Mark where platelets are.
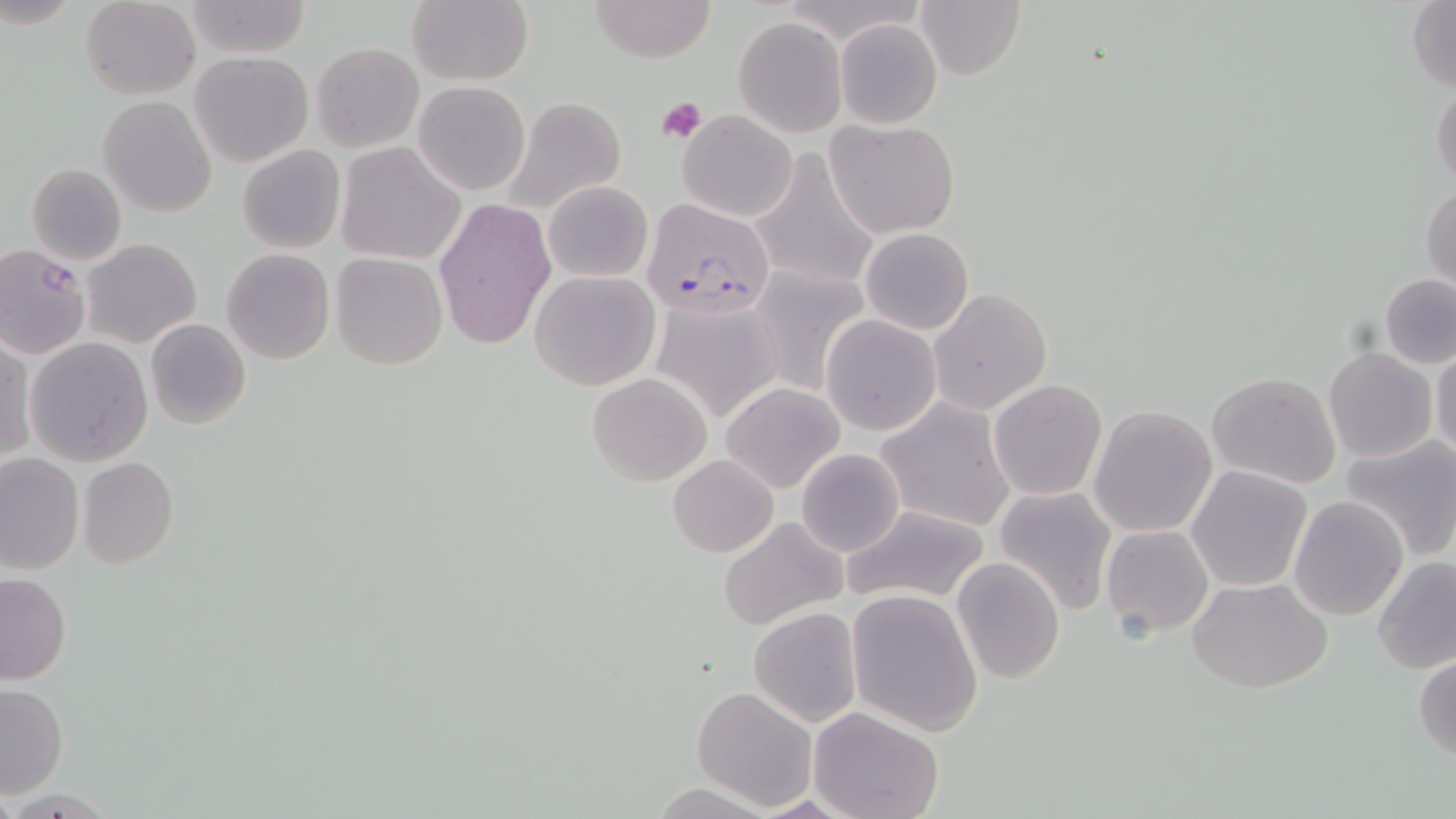
Approximate bounding boxes as [x1, y1, x2, y2] in pixels.
Platelets: [655, 95, 707, 144].

Uninfected red blood cell locations: [79, 0, 201, 99], [406, 0, 533, 86], [586, 0, 717, 62], [183, 1, 310, 61], [915, 1, 1025, 81], [1405, 1, 1455, 93], [732, 17, 847, 137], [833, 18, 942, 129], [311, 42, 423, 152], [190, 52, 314, 166], [414, 81, 530, 196], [1430, 81, 1456, 191], [98, 96, 216, 217], [500, 96, 629, 214], [676, 109, 798, 223], [826, 119, 959, 239], [335, 142, 465, 266], [236, 144, 346, 255], [748, 146, 879, 292], [27, 163, 126, 263], [543, 181, 652, 283], [1421, 184, 1455, 292], [435, 198, 556, 350], [860, 228, 974, 334], [81, 238, 202, 348], [0, 244, 92, 358], [221, 248, 335, 364], [330, 254, 448, 369], [750, 266, 871, 397], [529, 270, 659, 390], [1378, 273, 1456, 369], [927, 287, 1053, 415], [649, 296, 783, 423], [820, 314, 940, 436], [145, 318, 251, 430], [25, 337, 152, 466], [0, 339, 34, 464], [1431, 345, 1456, 460], [1323, 346, 1438, 464], [1207, 371, 1342, 489], [587, 373, 713, 486], [719, 381, 844, 493], [988, 381, 1107, 501], [875, 398, 1017, 532], [1088, 405, 1217, 537], [1340, 436, 1456, 561], [795, 448, 906, 558], [668, 454, 778, 558], [0, 455, 84, 576], [78, 458, 179, 568], [1187, 466, 1312, 590], [992, 485, 1119, 614], [1289, 496, 1407, 620], [842, 503, 993, 606], [718, 516, 846, 630], [1100, 523, 1214, 638], [1373, 556, 1456, 674], [952, 558, 1066, 684], [0, 573, 72, 684], [1190, 577, 1333, 692], [847, 589, 984, 735], [748, 607, 863, 727], [1414, 653, 1456, 764], [0, 684, 68, 797], [690, 685, 817, 811], [810, 708, 945, 819]. Plasmodium falciparum-infected red blood cell locations: [644, 198, 777, 319]. Slide-level diagnosis: Plasmodium falciparum. Thin blood smear. May-Grünwald-Giemsa stain. Image is 1456×819 pixels. One field of a larger specimen. Optical microscopy. Captured at 1000x magnification.